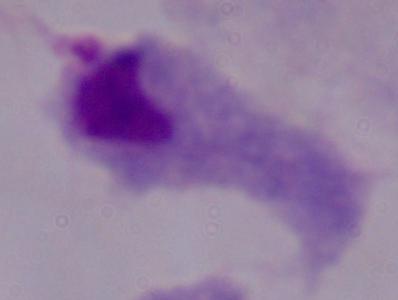 A trichomonad is shown. Photomicrograph. Captured at 1000x magnification.